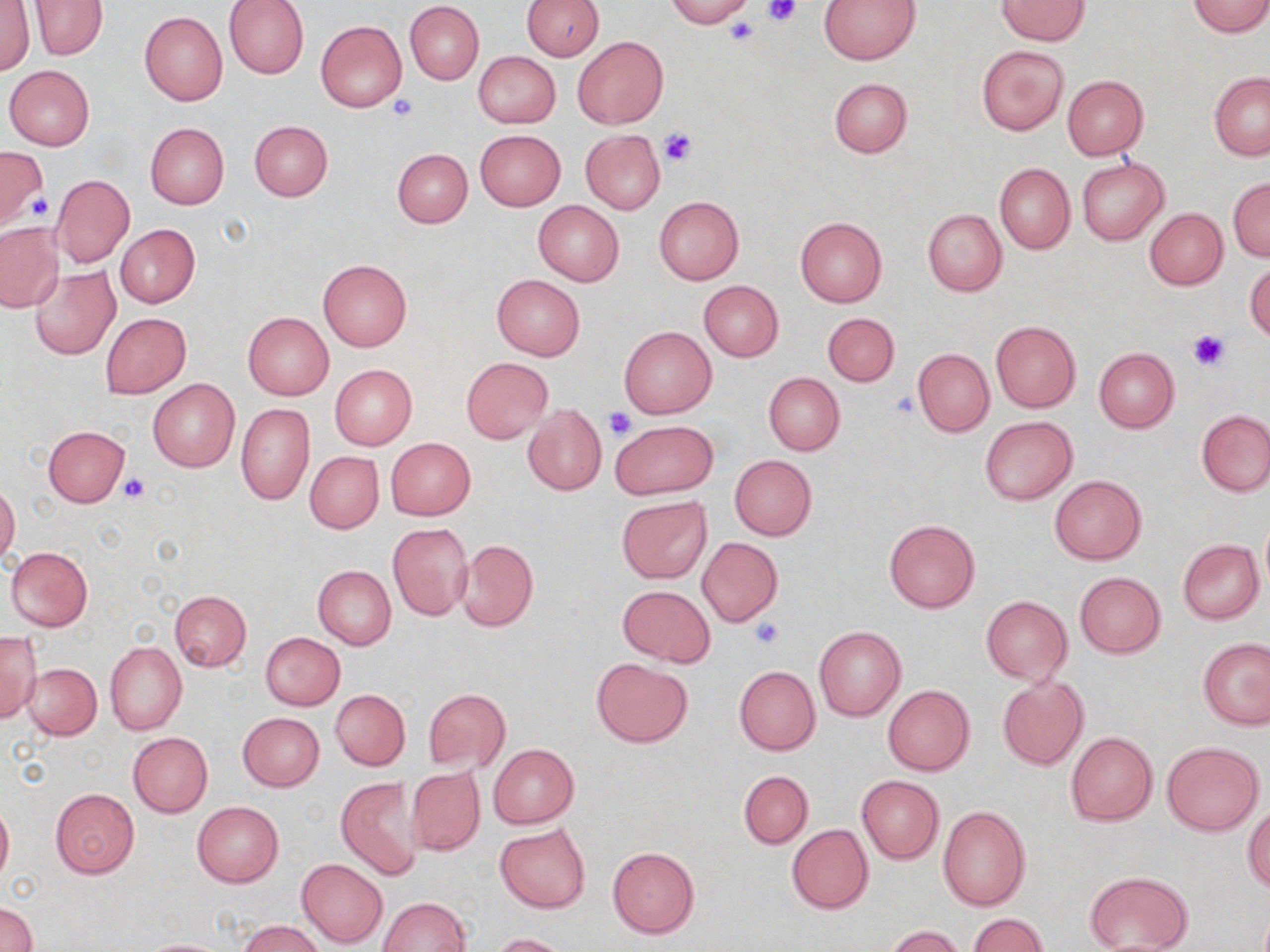 Approximate bounding boxes as (x1,y1)-(x2,y2) corner pairs in pixels. Uninfected red blood cell locations: (224,0)-(308,80), (521,0)-(604,60), (665,0)-(754,26), (818,0)-(920,64), (998,0)-(1087,45), (1,1)-(34,76), (32,1)-(106,59), (1187,1)-(1270,37), (404,3)-(484,84), (139,11)-(228,106), (316,20)-(406,112), (573,36)-(667,129), (976,45)-(1067,135), (473,51)-(559,128), (4,65)-(95,150), (1208,73)-(1270,160), (1061,75)-(1149,159), (828,78)-(912,158), (249,120)-(333,201), (145,122)-(229,208), (474,130)-(566,210), (581,130)-(665,214), (0,147)-(47,229), (392,148)-(473,228), (1077,157)-(1169,245), (994,163)-(1074,254), (49,175)-(135,268), (944,175)-(1071,273), (1228,177)-(1270,262), (654,196)-(743,284), (533,201)-(623,286), (1144,208)-(1227,290), (923,209)-(1006,296), (796,217)-(887,308), (0,224)-(64,312), (116,224)-(200,308), (1245,258)-(1270,344), (318,259)-(412,352), (30,267)-(119,359), (492,275)-(585,359), (699,280)-(783,361), (243,311)-(334,400), (100,312)-(191,397), (822,312)-(899,386), (991,320)-(1080,412), (619,326)-(716,418), (1093,347)-(1179,433), (912,348)-(994,436), (461,358)-(552,443), (329,364)-(417,450), (763,372)-(845,455), (148,378)-(239,472), (236,403)-(314,505), (523,405)-(607,495), (1197,409)-(1270,496), (980,416)-(1077,504), (610,420)-(716,500), (43,425)-(130,507), (385,438)-(476,519), (306,452)-(384,534), (729,454)-(817,540), (1050,475)-(1146,565), (0,482)-(20,565), (617,497)-(714,582), (1259,518)-(1270,594), (884,520)-(979,613), (387,523)-(473,620), (697,537)-(784,626), (1177,539)-(1264,624), (455,540)-(537,630), (6,546)-(92,631), (313,565)-(396,649), (1074,572)-(1166,658), (618,586)-(714,667), (169,590)-(251,671), (981,596)-(1072,685), (814,625)-(905,721), (0,631)-(42,721), (260,632)-(345,709), (1199,637)-(1270,730), (105,641)-(186,735), (591,657)-(693,748), (24,663)-(101,739), (734,665)-(821,755), (997,678)-(1088,770), (882,685)-(975,776), (422,688)-(511,773), (330,690)-(410,769), (238,712)-(324,791), (128,732)-(213,817), (1065,732)-(1157,825), (1162,742)-(1263,835), (488,743)-(579,828), (407,767)-(484,856), (738,770)-(813,849), (857,776)-(943,864), (335,777)-(427,880), (49,787)-(141,879), (0,798)-(13,886), (191,802)-(284,887), (938,805)-(1032,911), (1243,806)-(1270,893), (495,823)-(591,913), (786,824)-(873,913), (608,846)-(699,937), (297,858)-(388,948), (1083,870)-(1193,952), (376,897)-(471,952), (1,902)-(36,952), (969,913)-(1049,952), (240,919)-(326,952), (883,925)-(964,952), (492,932)-(573,952), (136,938)-(235,951). Platelet locations: (763,0)-(801,26), (726,16)-(758,45), (384,94)-(419,122), (657,128)-(697,165), (17,188)-(52,225), (1189,330)-(1228,372), (892,391)-(921,418), (603,407)-(637,442), (119,473)-(149,502), (751,616)-(783,648). Slide-level diagnosis: no evidence of blood parasites. Light microscopy. Captured at 1000x magnification. Thin blood film. Image is 1270×952 pixels. May-Grünwald-Giemsa-stained preparation. Single field of view.